State the preparation type.
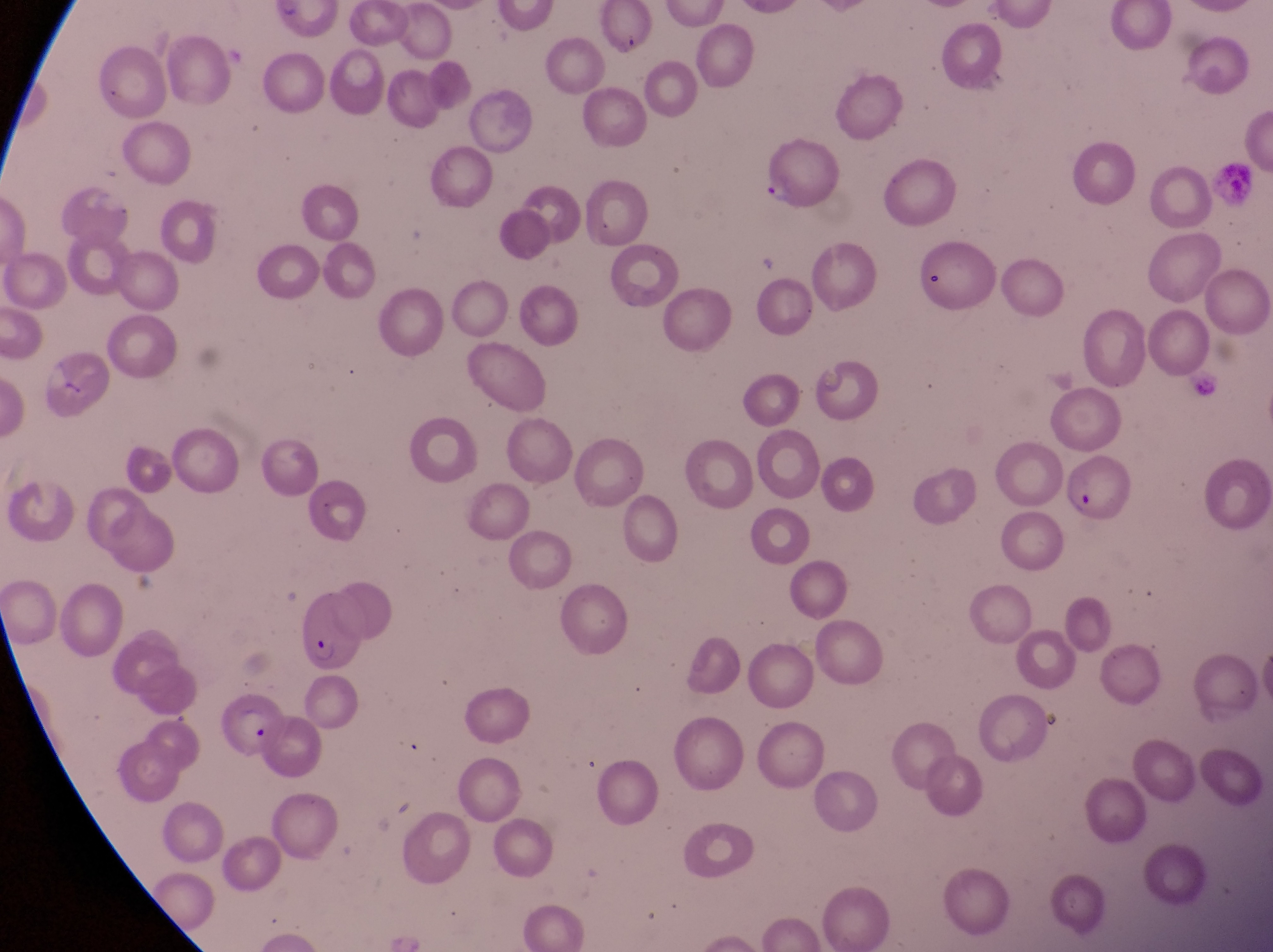
Thin blood smear.

country = Uganda
capture = smartphone photograph through the eyepiece of an Olympus CX-23 microscope
field of view = single
parasitised red blood cell locations = approximate bounding boxes as {left, top, right, bottom} in pixels: {1212, 155, 1259, 206}, {1064, 456, 1133, 523}, {289, 596, 361, 678}, {220, 700, 283, 760}
magnification = 1000x
image size = 1273×952 pixels
trophozoite locations = approximate bounding boxes as {left, top, right, bottom} in pixels: {759, 172, 798, 209}